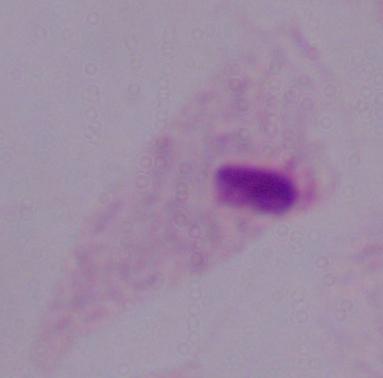

Summary:
  - Magnification: 1000x
  - Identification: trichomonad
  - Modality: micrograph